Locate and identify every blood parasite.
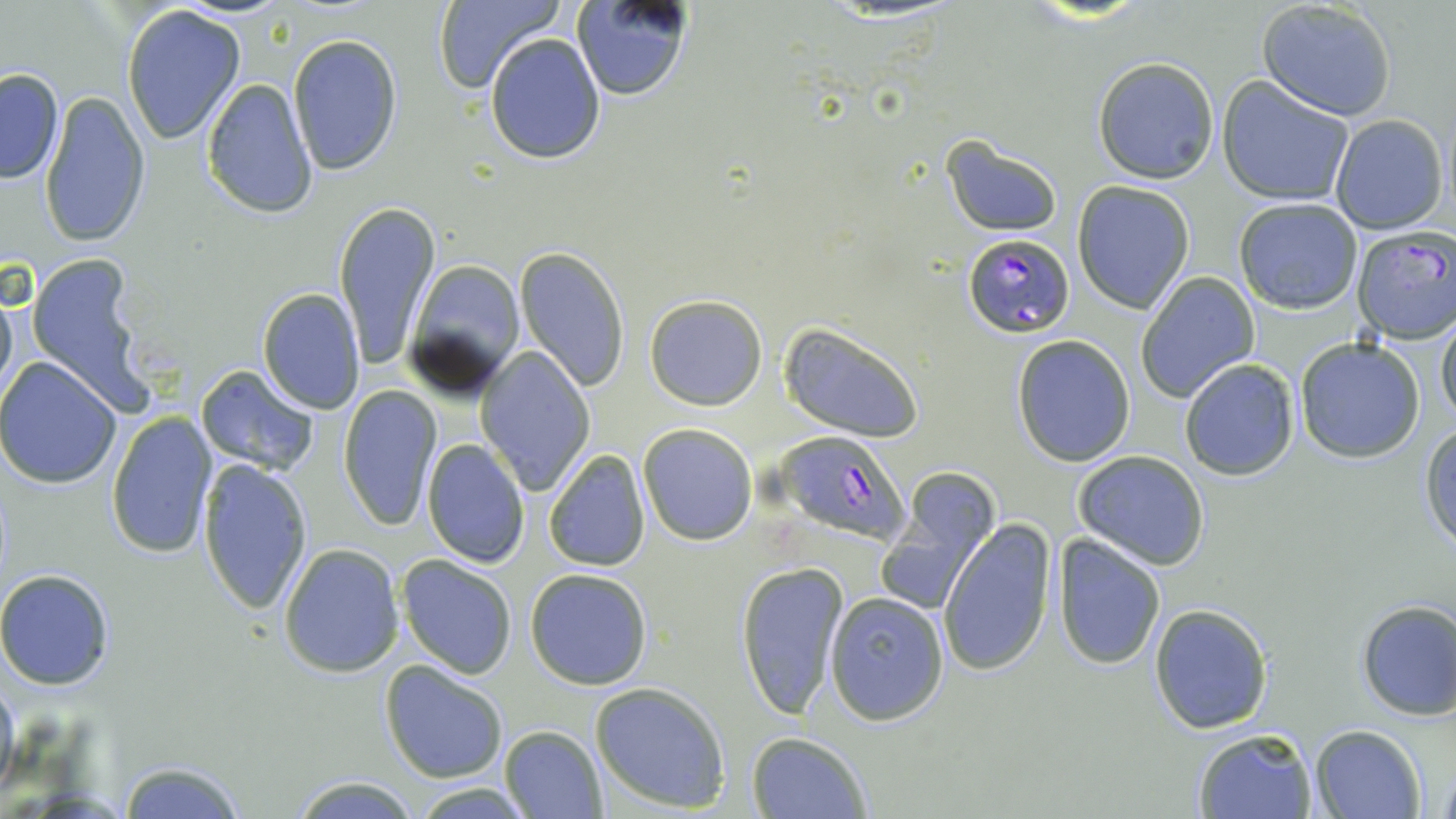
Approximate bounding boxes as (x1, y1, x2, y2) in pixels.
Plasmodium falciparum-infected red blood cells: (1351, 225, 1455, 342), (963, 235, 1074, 337), (780, 429, 911, 545).
No Plasmodium ovale, Plasmodium malariae, Plasmodium vivax, Babesia divergens, or Trypanosoma brucei observed.

Uninfected red blood cell locations: (433, 0, 564, 95), (571, 0, 697, 103), (1255, 3, 1397, 121), (120, 4, 247, 145), (287, 34, 403, 177), (485, 34, 606, 164), (1092, 56, 1220, 184), (0, 67, 64, 184), (203, 77, 318, 220), (1217, 78, 1354, 205), (40, 91, 150, 247), (1330, 114, 1449, 235), (941, 134, 1065, 236), (1073, 182, 1195, 313), (1233, 198, 1363, 315), (333, 199, 441, 371), (513, 245, 632, 393), (25, 257, 150, 412), (404, 257, 525, 396), (1136, 272, 1259, 403), (256, 287, 366, 414), (0, 291, 18, 407), (645, 294, 768, 411), (1436, 311, 1456, 429), (779, 322, 926, 442), (1011, 335, 1137, 466), (1294, 338, 1426, 464), (475, 349, 595, 495), (1179, 357, 1299, 481), (0, 358, 123, 488), (195, 364, 321, 478), (338, 388, 442, 530), (106, 410, 217, 559), (638, 422, 758, 545), (1420, 424, 1456, 554), (423, 438, 530, 570), (543, 449, 650, 572), (1073, 451, 1211, 569), (195, 456, 315, 616), (877, 474, 999, 614), (940, 520, 1058, 675), (1051, 534, 1168, 670), (277, 544, 404, 677), (397, 554, 520, 678), (734, 558, 851, 721), (524, 567, 654, 690), (0, 568, 115, 690), (823, 591, 949, 723), (1353, 599, 1456, 722), (1148, 602, 1273, 734), (381, 662, 508, 784), (0, 676, 21, 803), (590, 681, 733, 813), (499, 726, 607, 818), (1310, 726, 1426, 818), (1192, 728, 1317, 818), (747, 732, 871, 819), (116, 760, 249, 818), (1431, 762, 1455, 817), (286, 774, 420, 817), (412, 782, 532, 817). Slide-level diagnosis: Plasmodium falciparum. Thin blood film. Image is 1456×819 pixels. 1000x magnification. Optical microscopy. May-Grünwald-Giemsa stain. Single field of view.